Assess this cell for malaria.
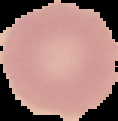

It is uninfected.

The area outside the segmented cell region is set to black. From a thin blood film. Image is 118×121 pixels.